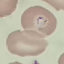
Summary:
  - Malaria status: parasitized
  - Preparation: thin blood smear
  - Image type: automatically extracted cell patch, resized to 64 × 64 pixels
  - Stain: Giemsa
  - Capture: smartphone camera at the microscope eyepiece